Assess this cell for malaria.
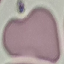

Uninfected.

Thin blood smear. Acquired by smartphone through the microscope eyepiece. Cell patch, automatically extracted from a larger field of view and resized to 64 × 64 pixels. Giemsa stain.